Assess the morphology of the red blood cells.
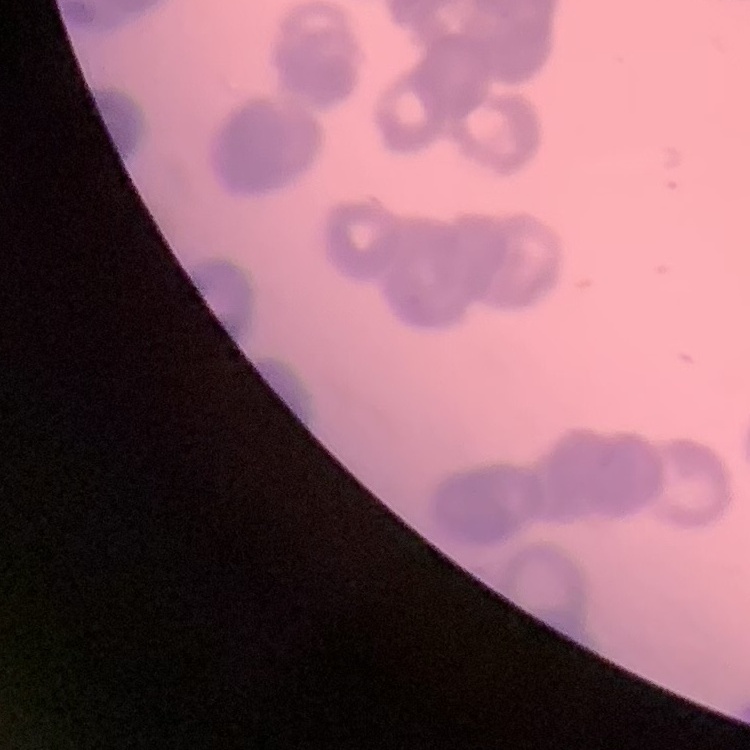

They show rouleaux formation.

{
  "preparation": "thin blood film",
  "image_type": "one tile cut from a larger photomicrograph",
  "stain": "Field's or Giemsa"
}